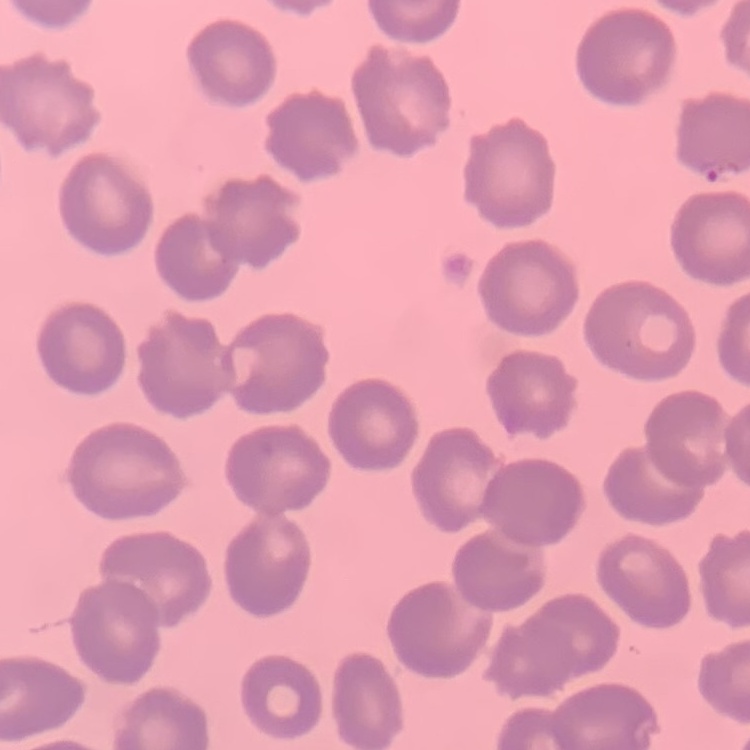
erythrocyte_morphology: no rouleaux formation
preparation: thin blood smear
image_type: one tile cut from a larger photomicrograph
stain: Field's or Giemsa